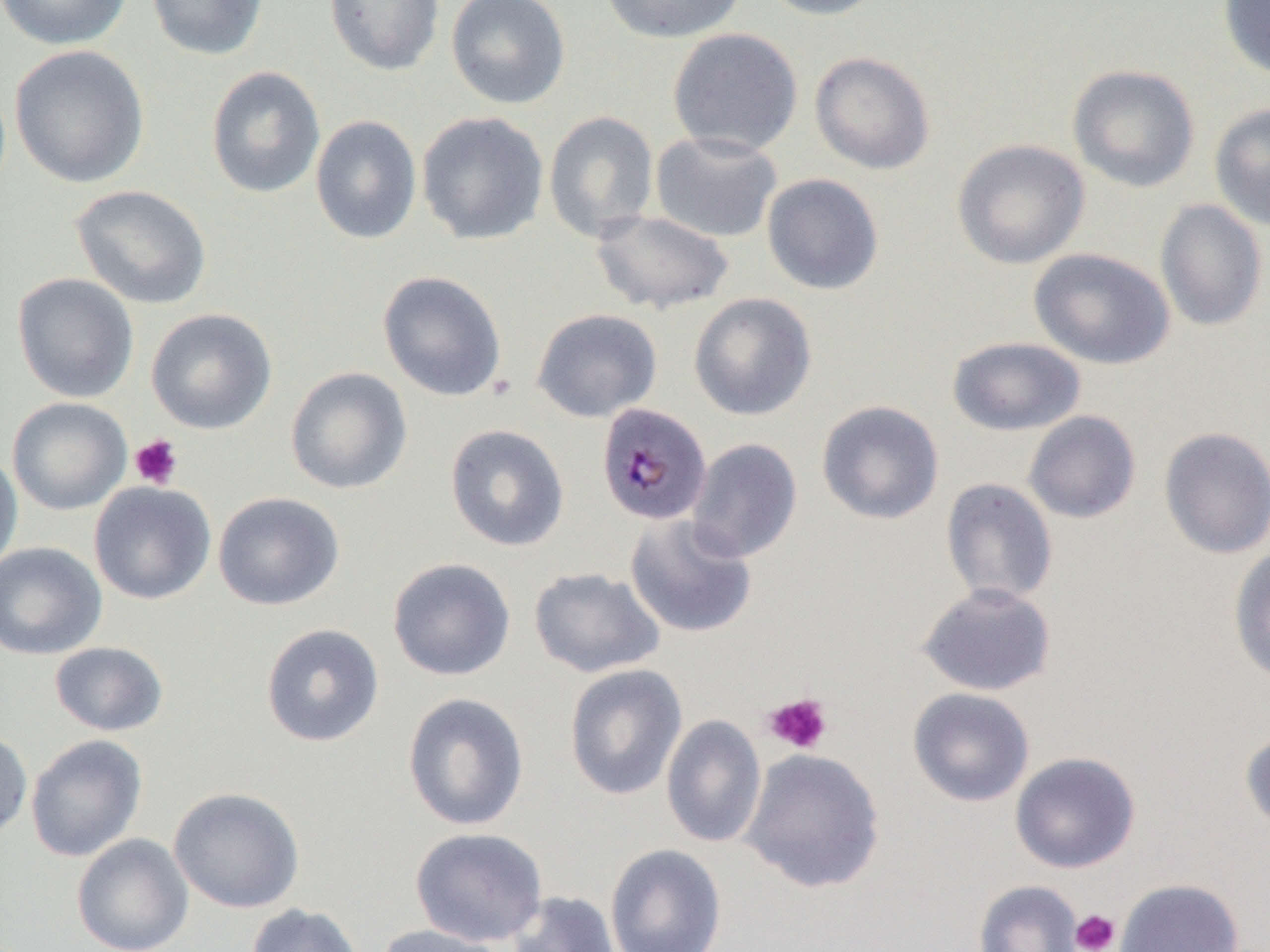
Approximate bounding boxes as (x1,y1)-(x2,y2) corner pairs in pixels. Platelet locations: (129,434)-(183,489), (763,692)-(833,755), (1070,909)-(1120,952). Uninfected red blood cell locations: (0,0)-(132,51), (146,0)-(269,61), (324,0)-(445,76), (446,0)-(571,109), (598,0)-(746,44), (756,0)-(889,20), (1217,0)-(1270,81), (667,27)-(803,156), (9,45)-(150,189), (809,51)-(936,175), (1067,64)-(1200,193), (206,66)-(326,199), (1209,102)-(1270,232), (543,110)-(660,243), (416,111)-(549,246), (310,115)-(422,244), (650,131)-(784,243), (952,138)-(1090,269), (761,173)-(885,295), (70,184)-(213,310), (1154,199)-(1268,332), (590,208)-(735,314), (1028,247)-(1175,370), (377,270)-(508,402), (12,272)-(139,403), (688,293)-(817,421), (145,307)-(278,434), (531,308)-(662,422), (947,336)-(1087,436), (285,366)-(413,495), (7,397)-(132,515), (816,400)-(944,525), (1023,410)-(1142,524), (444,423)-(570,552), (1158,426)-(1270,559), (686,438)-(803,564), (0,450)-(23,577), (940,478)-(1059,606), (89,481)-(217,605), (213,491)-(345,610), (624,514)-(757,638), (0,542)-(107,659), (1228,545)-(1270,685), (387,557)-(516,681), (528,566)-(665,678), (916,582)-(1057,696), (260,623)-(384,747), (49,641)-(169,737), (564,663)-(687,800), (907,687)-(1035,807), (402,692)-(530,831), (661,714)-(766,849), (0,728)-(33,841), (1239,728)-(1270,837), (26,734)-(147,862), (740,748)-(886,894), (1009,751)-(1141,873), (168,786)-(306,913), (410,826)-(549,947), (72,833)-(194,952), (605,844)-(727,952), (1115,878)-(1244,952), (972,879)-(1084,952), (505,890)-(621,952), (245,903)-(365,952), (374,923)-(508,952). Plasmodium malariae-infected red blood cell locations: (595,402)-(712,526). Slide-level diagnosis: Plasmodium malariae. Thin blood smear. Single field of view. Image is 1270×952 pixels. Optical microscopy. Captured at 1000x magnification.